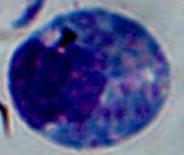
Photomicrograph. A white blood cell is shown. 1000x magnification.